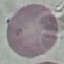
Summary:
  - Result: no malaria parasites seen
  - Stain: Giemsa
  - Capture: smartphone camera at the microscope eyepiece
  - Preparation: thin blood film
  - Image type: automatically extracted cell patch, resized to 64 × 64 pixels